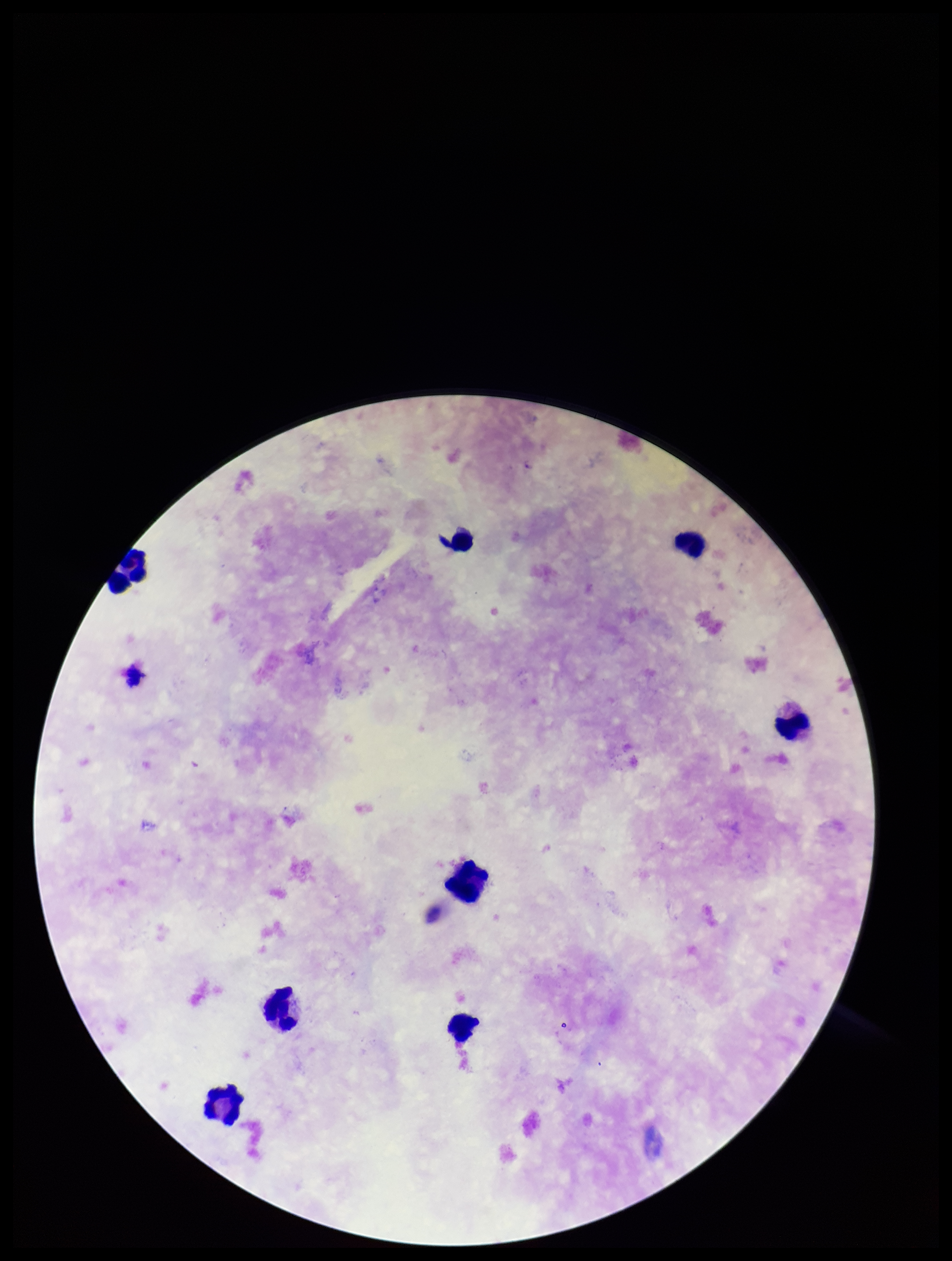

Parasite count: 1. Stained with Giemsa. Image is 952×1261 pixels. Plasmodium parasites: identified. Patient malaria status: infected. Leukocyte count: 8. Species reported for this patient: Plasmodium falciparum. Preparation: thick blood smear. Smartphone photograph taken through the eyepiece of a microscope. One field from this slide.